Report the malaria status of this cell.
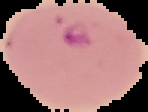
Parasitized.

Image is 148×112 pixels. Segmented cell region on a black background. From a thin blood smear.